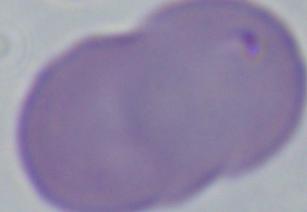
magnification = 1000x
identification = Babesia
modality = photomicrograph